Classify this cell by malaria status.
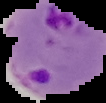

Parasitized.

Segmented cell region on a black background. From a thin blood smear. Image is 106×103 pixels.